Point out each leukocyte.
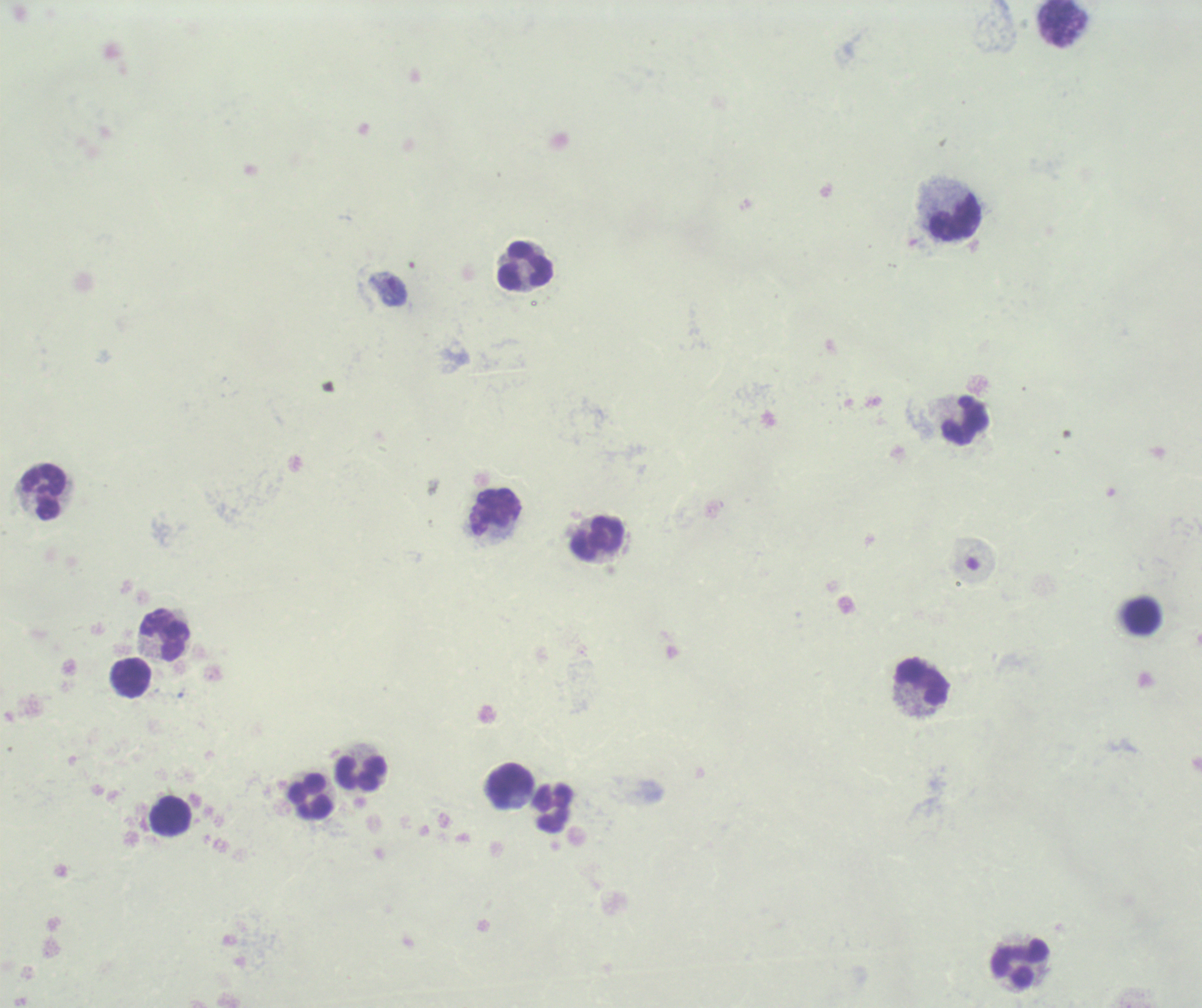

Approximate centers as [x, y] in pixels.
Leukocytes: [955, 217], [524, 266], [965, 420], [44, 491], [494, 513], [596, 537], [1141, 615], [165, 633], [130, 677], [923, 682], [361, 773], [509, 786], [311, 798], [554, 807], [171, 817], [1019, 962].

Approximate centers as [x, y] in pixels. Gametocyte locations: [388, 289]. Thick blood film. 100x magnification. Background quality: unsatisfactory. Result: positive for Plasmodium parasites. Image is 1202×1008 pixels. Previously used in a real diagnosis. Romanowsky stain. Single field of view.